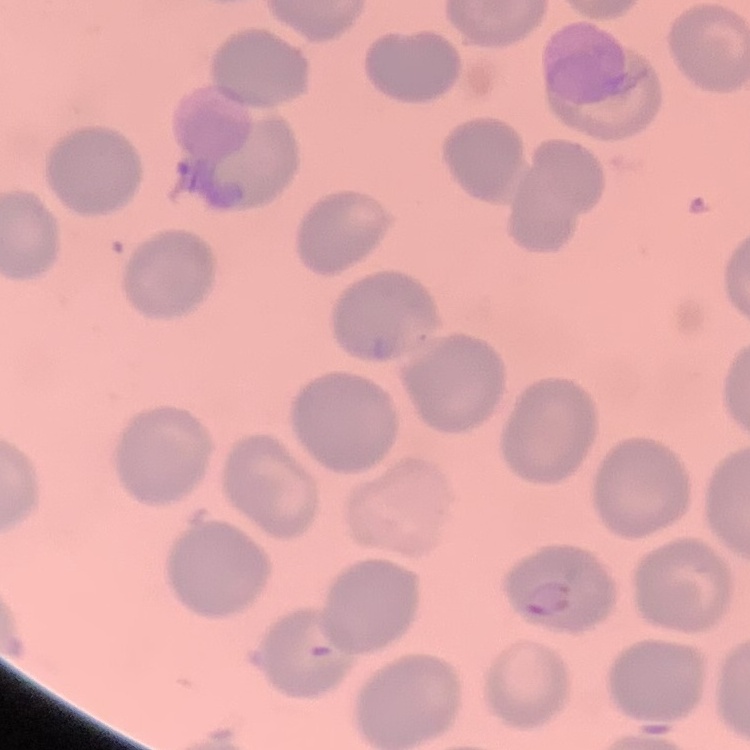

Summary:
  - Erythrocyte morphology: no rouleaux formation
  - Preparation: thin blood smear
  - Image type: one tile cut from a larger photomicrograph
  - Stain: Field's or Giemsa